State the blood parasite species.
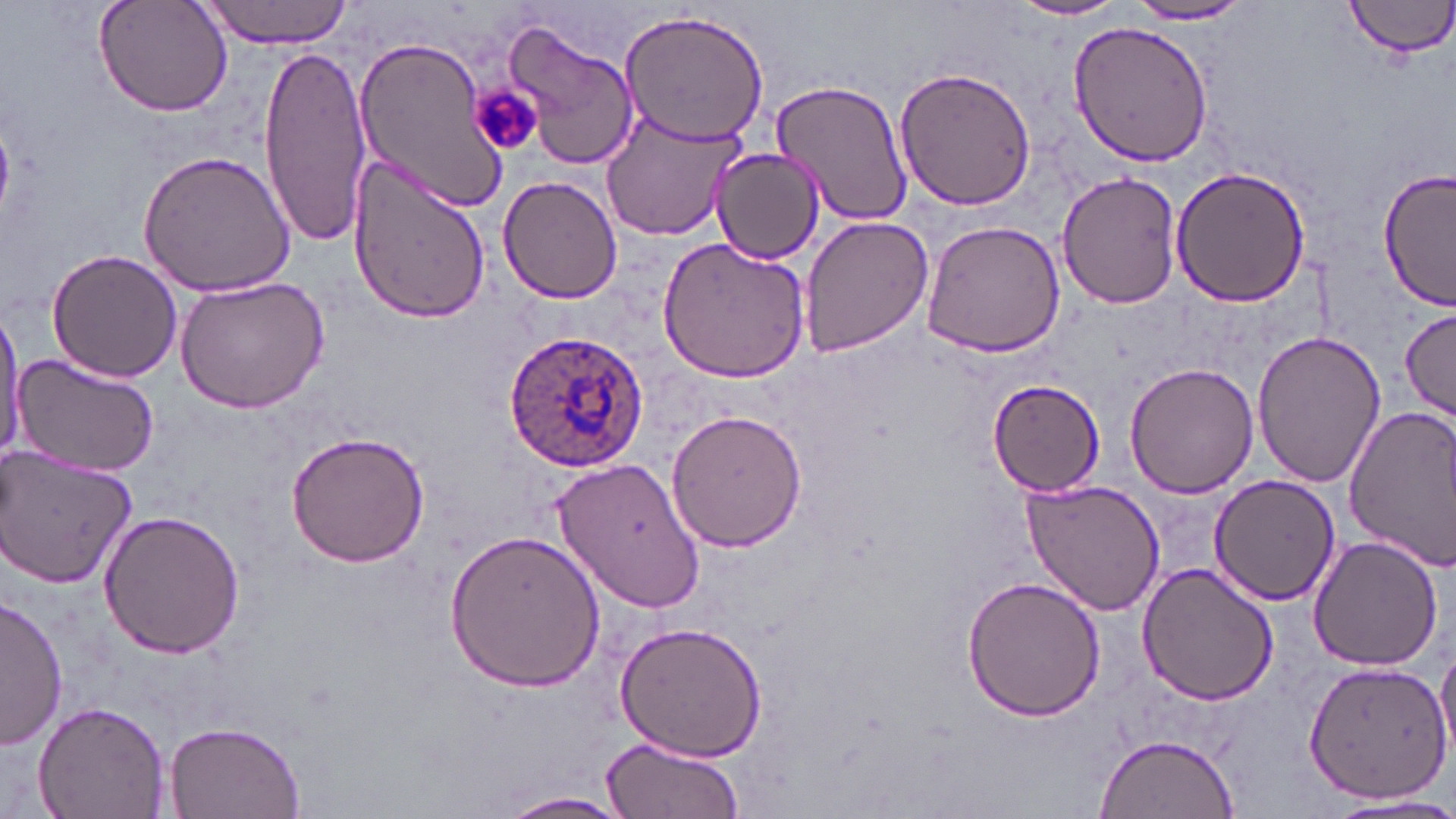

Plasmodium ovale.

modality = light microscopy
platelet locations = approximate bounding boxes as [x1, y1, x2, y2] in pixels: [471, 87, 540, 154]
field of view = one of a larger specimen
uninfected red blood cell locations = approximate bounding boxes as [x1, y1, x2, y2] in pixels: [94, 0, 233, 118], [199, 0, 356, 47], [1010, 0, 1129, 23], [1345, 0, 1456, 58], [1125, 3, 1259, 25], [618, 8, 772, 145], [496, 15, 640, 171], [1067, 19, 1213, 166], [353, 31, 511, 212], [258, 44, 373, 244], [895, 64, 1037, 211], [769, 76, 915, 228], [600, 110, 745, 241], [133, 146, 296, 297], [712, 147, 826, 264], [346, 150, 492, 328], [1169, 166, 1312, 307], [1377, 166, 1455, 311], [1056, 171, 1182, 307], [497, 175, 621, 303], [797, 215, 934, 357], [918, 219, 1065, 359], [656, 236, 811, 383], [47, 248, 185, 381], [173, 277, 329, 414], [1399, 307, 1454, 423], [0, 309, 24, 462], [1251, 329, 1386, 488], [10, 354, 161, 476], [1125, 362, 1259, 499], [989, 377, 1105, 496], [1343, 405, 1456, 573], [665, 406, 809, 550], [285, 429, 430, 569], [1, 446, 139, 588], [552, 456, 708, 614], [1209, 475, 1340, 607], [1021, 477, 1168, 618], [98, 510, 247, 660], [444, 530, 603, 692], [1307, 534, 1444, 670], [1137, 561, 1279, 705], [961, 576, 1105, 722], [0, 597, 69, 749], [611, 619, 767, 765], [1435, 642, 1456, 766], [1302, 661, 1453, 802], [33, 702, 168, 819], [162, 721, 308, 819], [1095, 734, 1240, 818], [602, 735, 742, 819], [501, 792, 629, 816], [1322, 793, 1456, 818]
stain = May-Grünwald-Giemsa
image size = 1456×819 pixels
magnification = 1000x
Plasmodium ovale-infected red blood cell locations = approximate bounding boxes as [x1, y1, x2, y2] in pixels: [503, 329, 649, 469]
preparation = thin blood film